Look for Plasmodium parasites.
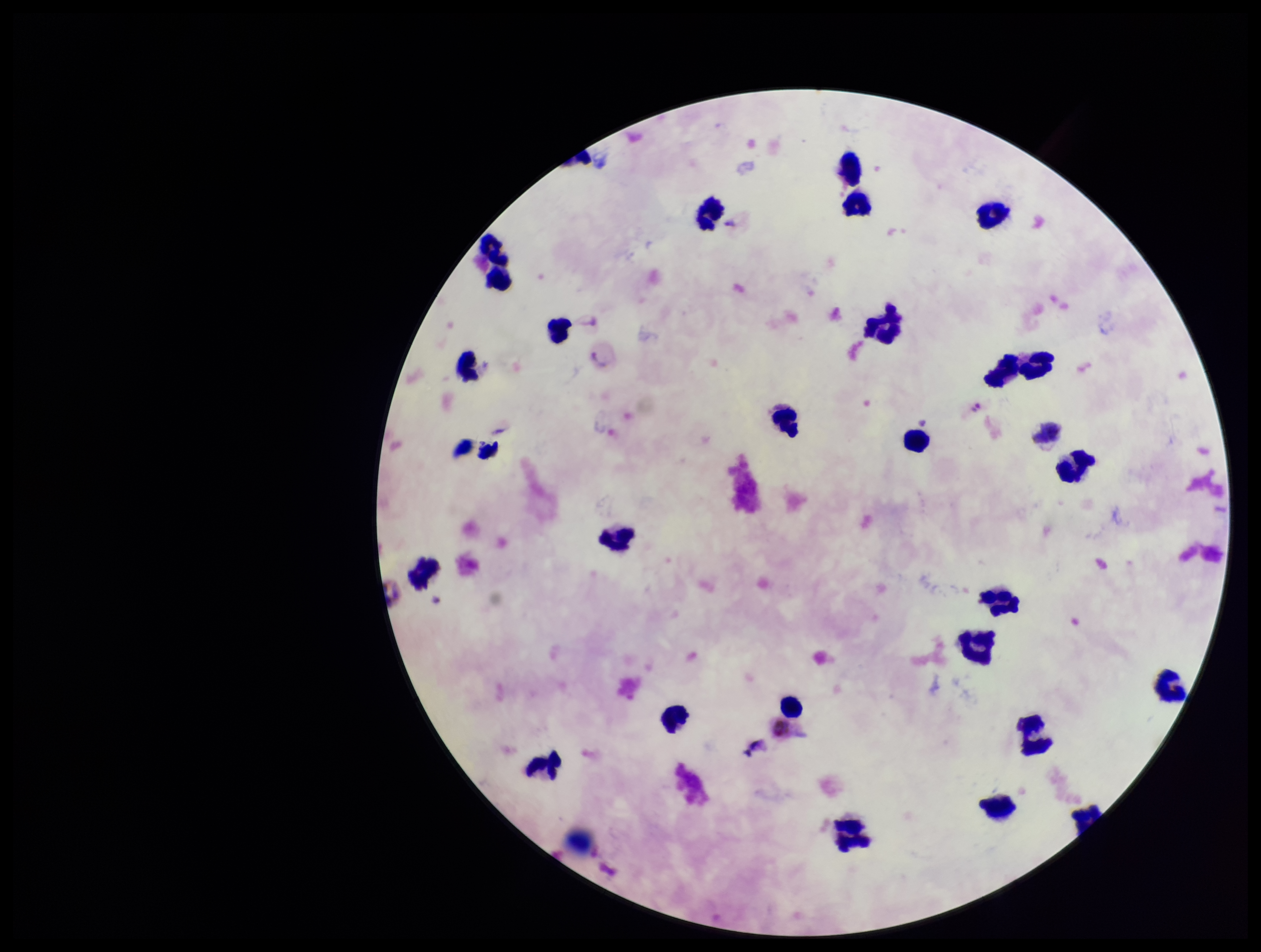

None seen.

preparation = thick
stain = Giemsa
species reported for this patient = Plasmodium vivax
leukocyte count = 24
image size = 1261×952 pixels
capture = smartphone photograph through the microscope eyepiece
patient malaria status = positive
field of view = single
parasite count = 0